Locate every Plasmodium parasite.
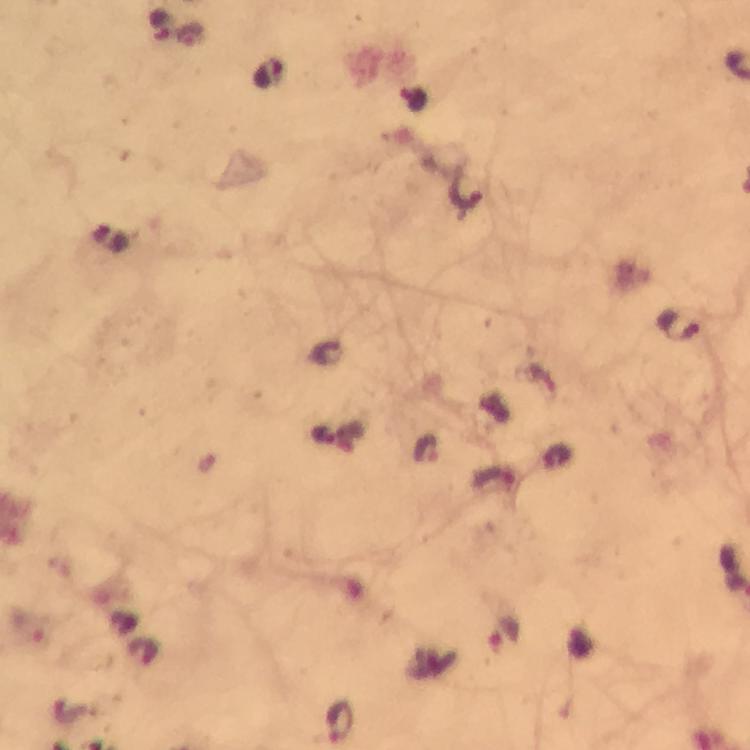
Approximate centers as [x, y] in pixels.
Plasmodium parasites: [161, 25], [191, 37], [268, 73], [414, 99], [680, 325], [426, 450], [496, 478], [507, 635], [341, 722].

stain = Giemsa
cropped from = one field of view
capture = smartphone camera through the microscope
immersion oil = used
context = from a diagnostic examination for malaria
preparation = thick blood smear
image size = 750×750 pixels
magnification = 100x